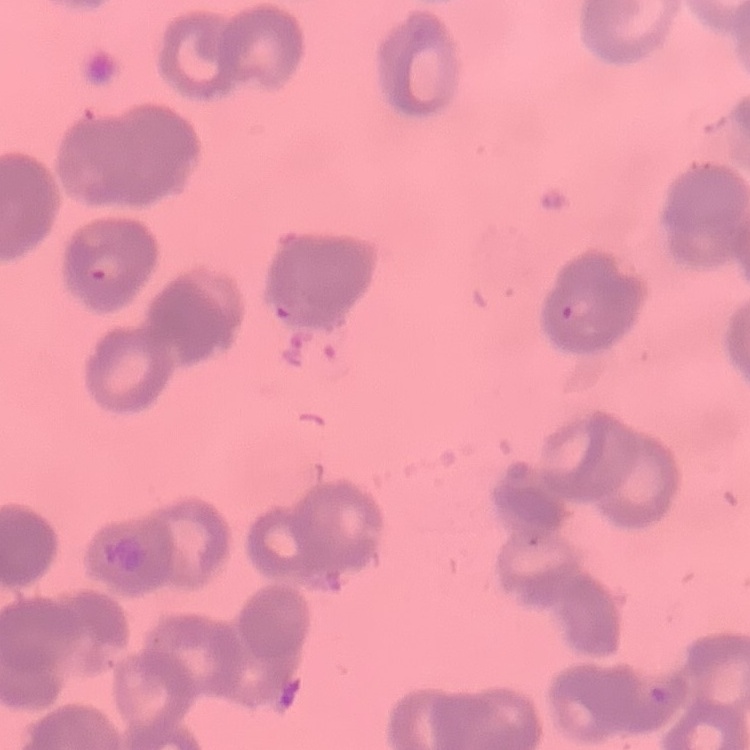
erythrocyte morphology = rouleaux formation
preparation = thin blood smear
stain = Field's or Giemsa
image type = square crop of a larger photomicrograph